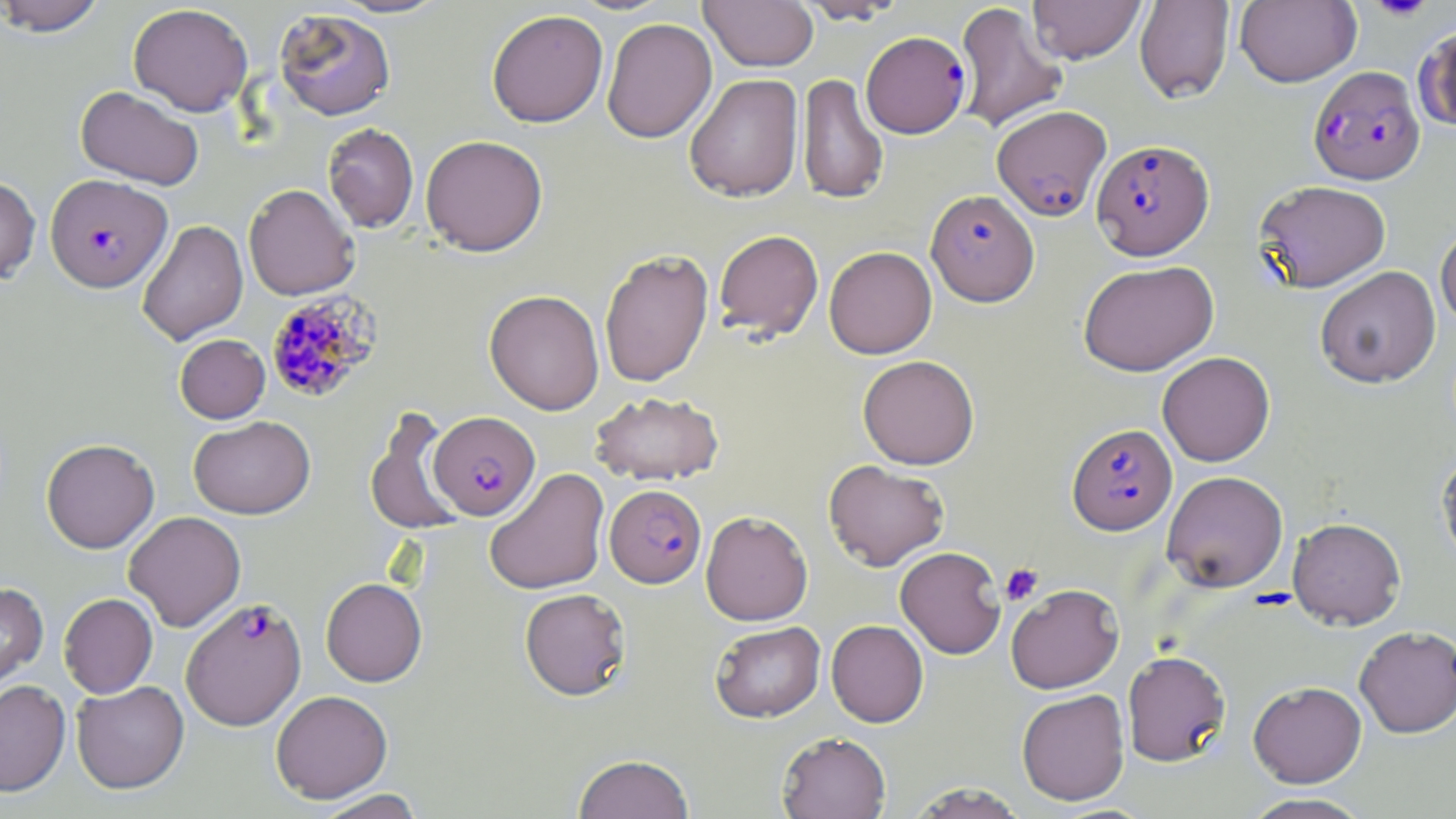

slide-level diagnosis = Plasmodium falciparum
preparation = thin blood film
image size = 1456×819 pixels
field of view = single
platelet locations = approximate bounding boxes as (x1, y1, x2, y2) in pixels: (1369, 0, 1434, 21), (1000, 563, 1043, 606)
modality = light microscopy
uninfected red blood cell locations = approximate bounding boxes as (x1, y1, x2, y2) in pixels: (0, 0, 108, 36), (329, 0, 452, 18), (701, 0, 818, 71), (795, 0, 908, 25), (1028, 0, 1146, 64), (1134, 0, 1235, 104), (1235, 0, 1361, 87), (954, 1, 1068, 133), (128, 3, 253, 116), (273, 8, 396, 120), (487, 9, 608, 127), (601, 17, 717, 143), (1414, 23, 1456, 131), (684, 73, 803, 202), (798, 73, 888, 205), (76, 86, 204, 190), (322, 123, 419, 232), (421, 134, 548, 256), (0, 175, 40, 285), (1254, 180, 1391, 292), (243, 184, 359, 301), (137, 220, 248, 345), (1434, 223, 1456, 330), (714, 229, 823, 341), (824, 246, 937, 358), (599, 247, 714, 388), (1078, 260, 1219, 376), (1315, 265, 1441, 388), (484, 289, 605, 415), (175, 334, 270, 423), (1157, 351, 1275, 467), (858, 355, 979, 469), (589, 391, 725, 486), (364, 409, 465, 536), (188, 416, 315, 519), (41, 438, 159, 553), (1436, 446, 1456, 574), (823, 459, 949, 571), (484, 468, 610, 596), (1162, 470, 1288, 592), (700, 510, 813, 625), (124, 511, 246, 631), (1287, 517, 1406, 630), (895, 546, 1006, 659), (321, 577, 427, 686), (0, 582, 48, 697), (1006, 584, 1124, 694), (520, 588, 631, 700), (59, 593, 158, 698), (826, 620, 928, 727), (710, 621, 826, 722), (1354, 625, 1456, 737), (1123, 650, 1231, 766), (0, 678, 70, 796), (71, 680, 189, 794), (1248, 680, 1367, 787), (1016, 689, 1130, 805), (271, 690, 393, 803), (777, 732, 891, 819), (573, 753, 695, 819), (906, 782, 1028, 818), (313, 789, 426, 819), (1239, 793, 1375, 819)
magnification = 1000x
Plasmodium falciparum-infected red blood cell locations = approximate bounding boxes as (x1, y1, x2, y2) in pixels: (861, 31, 970, 138), (1308, 66, 1425, 184), (992, 105, 1111, 221), (1091, 139, 1214, 260), (45, 174, 171, 292), (926, 189, 1040, 306), (265, 291, 382, 404), (429, 411, 540, 520), (1067, 423, 1177, 535), (605, 484, 706, 587), (180, 598, 307, 730)
stain = May-Grünwald-Giemsa